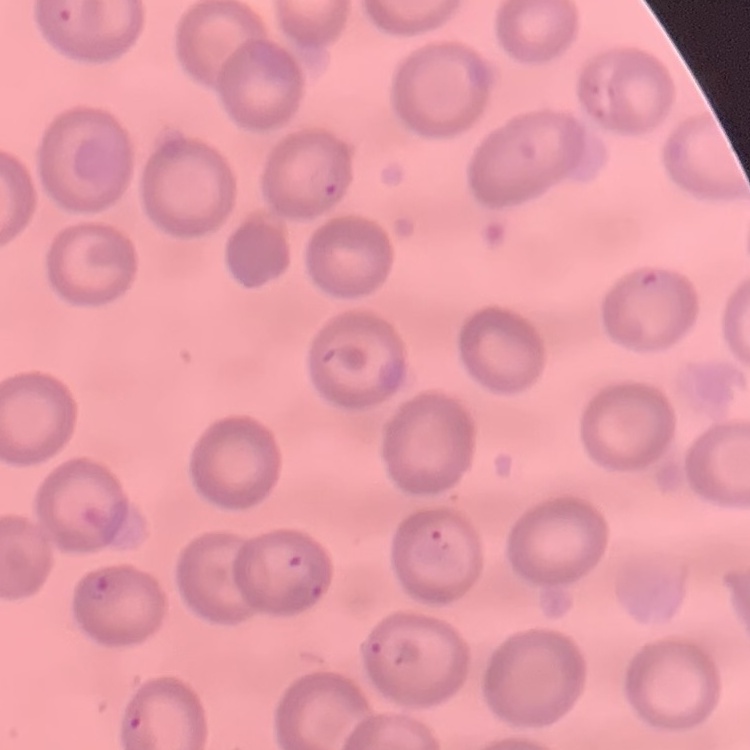
Summary:
  - Erythrocyte morphology: no rouleaux formation
  - Preparation: thin blood smear
  - Stain: Field's or Giemsa
  - Image type: one tile cut from a larger photomicrograph